Locate every uninfected red blood cell.
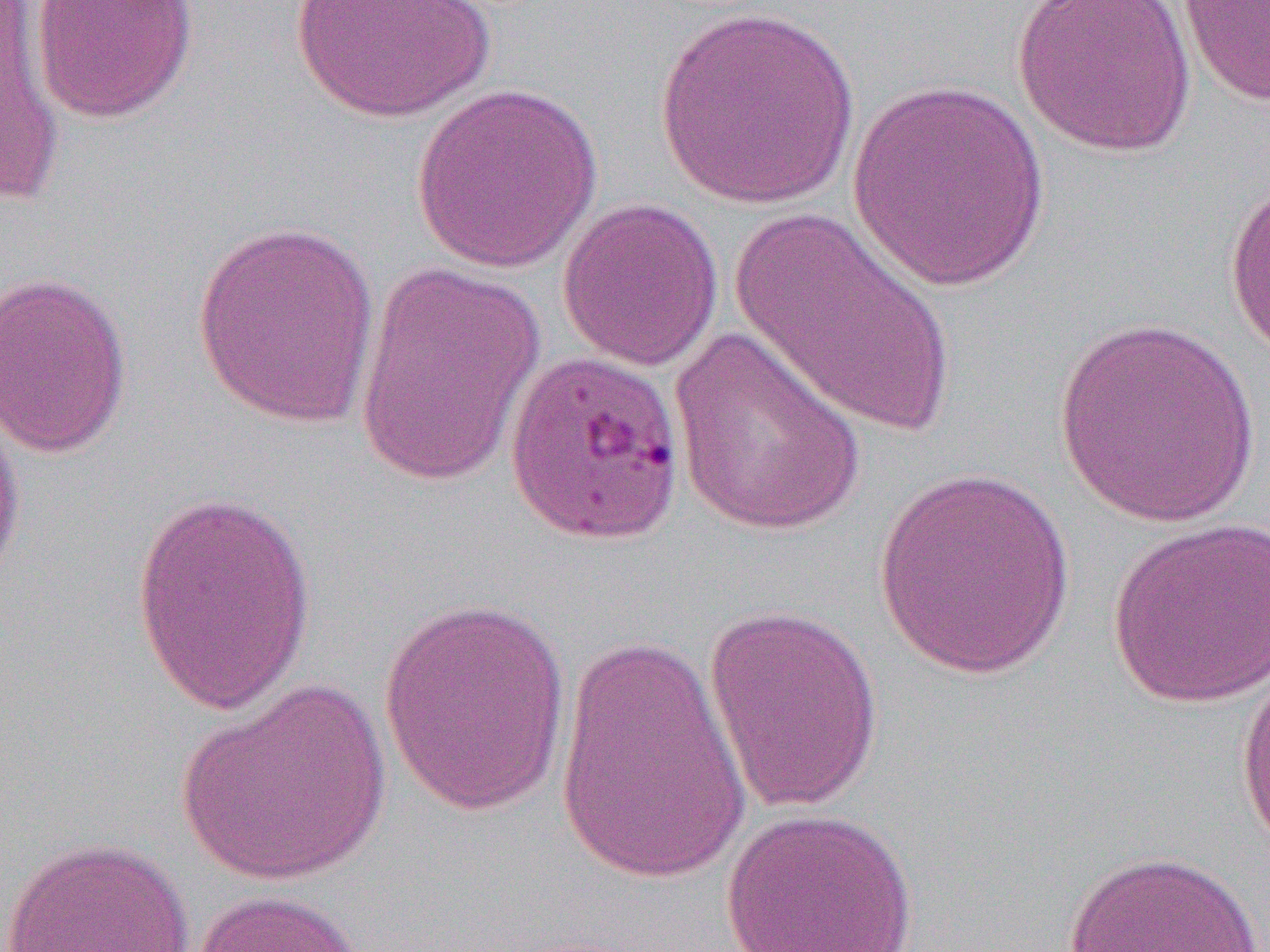

Approximate bounding boxes as [x1, y1, x2, y2] in pixels.
Uninfected red blood cells: [1, 0, 65, 209], [30, 0, 198, 124], [1012, 0, 1196, 157], [1176, 0, 1270, 109], [288, 1, 496, 122], [653, 5, 861, 210], [845, 80, 1053, 293], [410, 82, 604, 274], [1224, 175, 1270, 361], [557, 197, 723, 372], [730, 206, 958, 440], [191, 219, 384, 431], [352, 257, 549, 487], [0, 269, 134, 459], [1052, 317, 1262, 527], [667, 326, 871, 536], [0, 383, 27, 605], [873, 466, 1077, 680], [129, 489, 317, 717], [1106, 517, 1270, 708], [377, 595, 574, 819], [703, 602, 885, 817], [552, 630, 753, 890], [1234, 661, 1270, 858], [176, 680, 391, 887], [721, 807, 920, 952], [0, 836, 197, 951], [1060, 850, 1270, 952], [186, 889, 370, 952].

Slide-level diagnosis: Plasmodium falciparum. Thin blood smear. Single field of view. Image is 1270×952 pixels. Optical microscopy. 1000x magnification.